Locate every Plasmodium malariae-infected red blood cell.
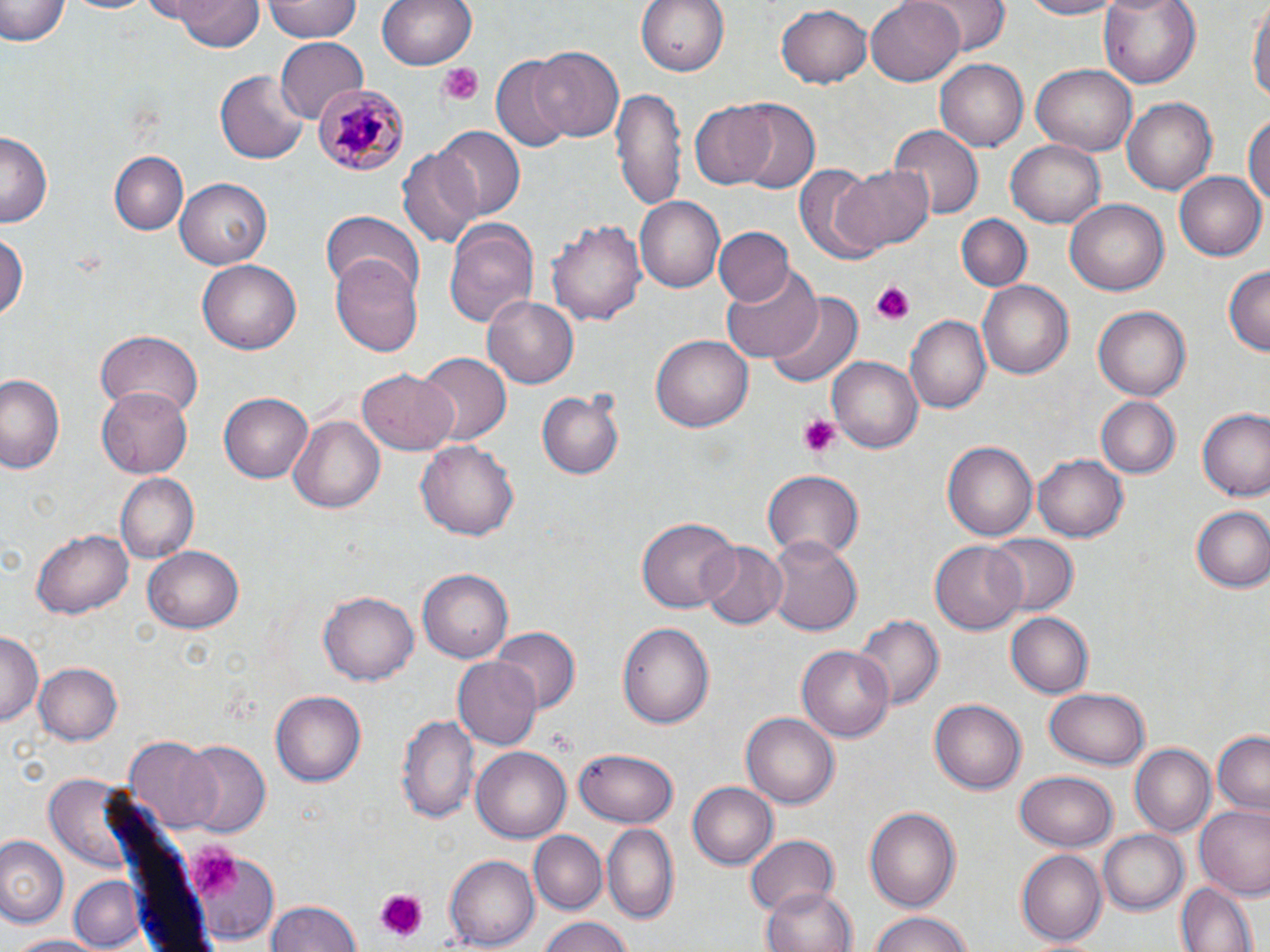
Approximate bounding boxes as [x1, y1, x2, y2] in pixels.
Plasmodium malariae-infected red blood cells: [310, 79, 407, 176].

{
  "slide_level_diagnosis": "Plasmodium malariae",
  "modality": "optical microscopy",
  "image_size": "1270×952 pixels",
  "magnification": "1000x",
  "stain": "May-Grünwald-Giemsa",
  "uninfected_red_blood_cell_locations": "approximate bounding boxes as [x1, y1, x2, y2] in pixels: [163, 0, 263, 50], [263, 0, 362, 42], [379, 0, 475, 71], [635, 0, 733, 74], [864, 0, 964, 85], [919, 0, 1007, 53], [1013, 0, 1130, 19], [1097, 0, 1202, 90], [1249, 0, 1268, 113], [0, 1, 66, 48], [775, 4, 872, 87], [274, 39, 367, 120], [530, 45, 624, 142], [491, 55, 573, 151], [935, 59, 1031, 151], [1032, 65, 1136, 156], [215, 69, 310, 165], [612, 87, 687, 209], [1123, 97, 1217, 195], [727, 102, 819, 193], [692, 103, 776, 190], [1246, 108, 1270, 217], [889, 126, 983, 218], [433, 127, 525, 218], [2, 132, 54, 228], [1007, 140, 1106, 228], [397, 147, 483, 250], [109, 152, 187, 234], [833, 163, 935, 253], [793, 164, 882, 266], [1174, 169, 1266, 261], [175, 177, 272, 270], [635, 196, 724, 293], [1066, 198, 1170, 296], [321, 210, 423, 298], [956, 213, 1032, 290], [547, 217, 647, 326], [444, 219, 538, 328], [712, 226, 794, 307], [0, 229, 26, 330], [329, 255, 422, 357], [197, 259, 300, 355], [720, 266, 820, 365], [1222, 266, 1269, 357], [977, 280, 1072, 380], [767, 292, 863, 392], [483, 295, 578, 389], [1094, 305, 1193, 400], [905, 313, 990, 414], [97, 331, 202, 419], [651, 334, 754, 433], [416, 352, 512, 446], [830, 356, 921, 455], [358, 366, 457, 453], [0, 370, 64, 477], [99, 385, 196, 479], [538, 386, 624, 480], [219, 391, 314, 484], [1094, 394, 1180, 479], [1198, 408, 1270, 503], [289, 416, 384, 511], [416, 437, 518, 538], [942, 440, 1038, 541], [1034, 451, 1132, 542], [762, 471, 864, 559], [115, 473, 198, 562], [1189, 506, 1270, 594], [638, 516, 737, 611], [32, 529, 135, 618], [982, 533, 1078, 617], [767, 534, 864, 638], [930, 538, 1027, 632], [696, 542, 787, 627], [144, 546, 244, 632], [418, 569, 512, 664], [319, 592, 418, 686], [1007, 613, 1093, 697], [854, 615, 942, 712], [618, 622, 715, 728], [489, 628, 578, 714], [0, 630, 41, 728], [799, 644, 894, 743], [453, 657, 542, 751], [34, 663, 123, 746], [1042, 687, 1153, 770], [271, 690, 370, 786], [929, 696, 1025, 791], [740, 710, 839, 810], [398, 713, 480, 824], [1211, 732, 1269, 815], [125, 735, 223, 831], [180, 741, 270, 840], [1128, 743, 1214, 836], [575, 746, 677, 825], [472, 747, 570, 842], [1014, 772, 1117, 851], [687, 781, 778, 869], [1194, 805, 1270, 901], [865, 806, 961, 908], [601, 821, 680, 922], [1099, 829, 1187, 912], [528, 830, 606, 914], [742, 834, 840, 916], [0, 836, 67, 927], [184, 846, 279, 944], [1016, 849, 1107, 945], [445, 854, 539, 950], [73, 874, 140, 947], [1176, 881, 1256, 952], [756, 884, 859, 952], [264, 898, 361, 952], [866, 910, 976, 952], [534, 917, 633, 952], [5, 934, 110, 951]",
  "field_of_view": "one of a larger specimen",
  "preparation": "thin blood film",
  "platelet_locations": "approximate bounding boxes as [x1, y1, x2, y2] in pixels: [439, 64, 484, 106], [870, 282, 917, 325], [797, 415, 841, 459], [545, 729, 573, 753], [185, 845, 242, 895], [373, 888, 428, 942]"
}